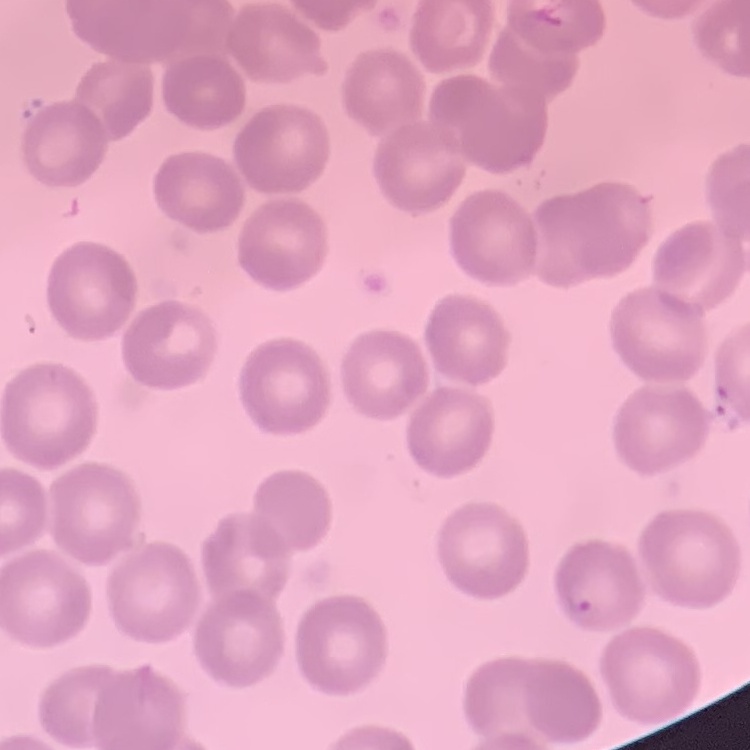

The red blood cells show no rouleaux formation. Field's or Giemsa stain. Thin blood smear. One tile cut from a larger photomicrograph.